Locate and identify every blood parasite.
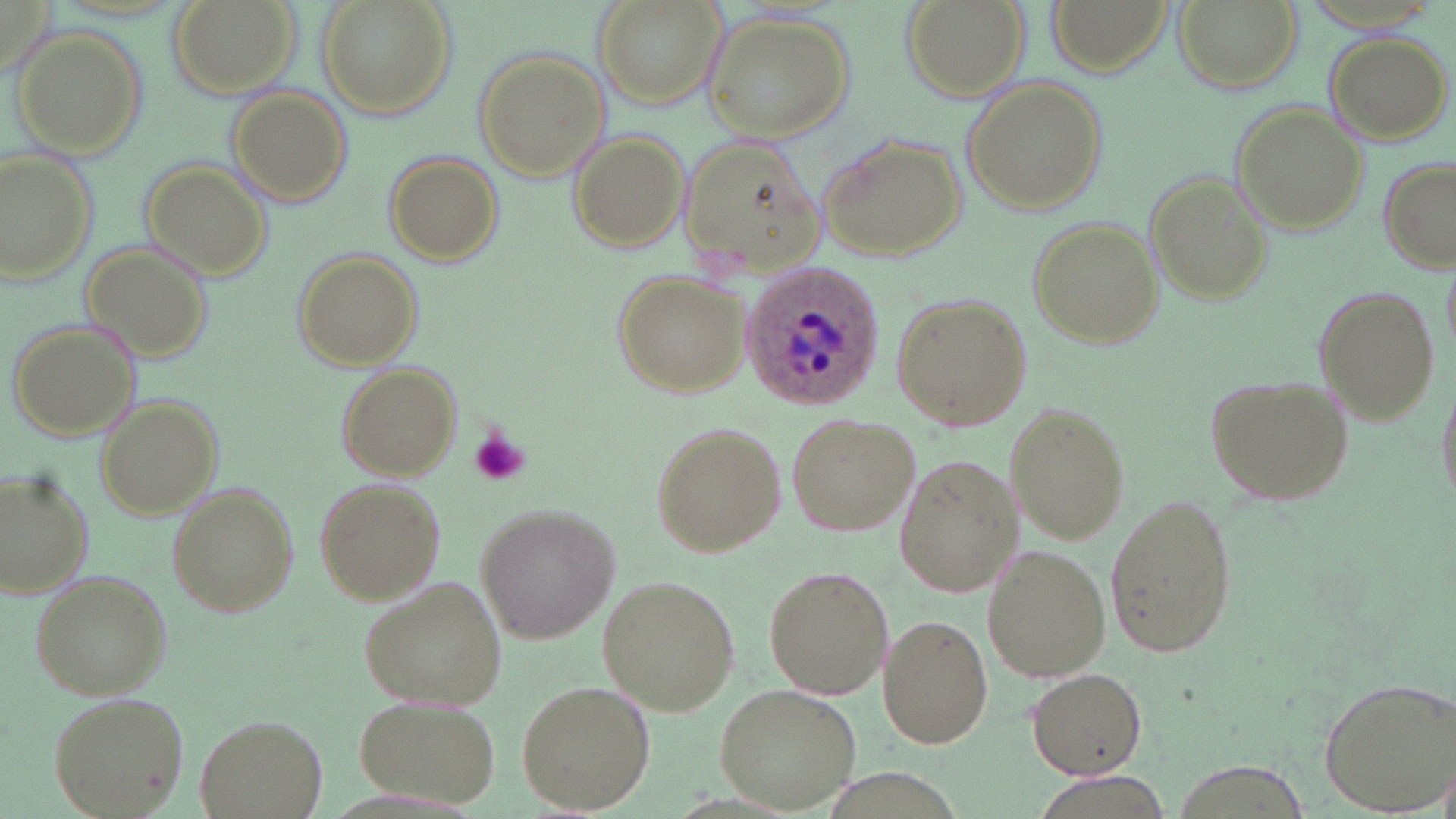
Approximate bounding boxes as (x1,y1)-(x2,y2) corner pairs in pixels.
Plasmodium ovale-infected red blood cells: (738,264)-(886,411).
No Plasmodium falciparum, Plasmodium malariae, Plasmodium vivax, Babesia divergens, or Trypanosoma brucei observed.

Platelet locations: (468,428)-(532,488). Uninfected red blood cell locations: (165,0)-(302,101), (317,0)-(456,118), (593,0)-(729,111), (900,0)-(1031,101), (1047,0)-(1171,77), (1173,0)-(1302,94), (700,6)-(853,142), (15,29)-(148,156), (1325,31)-(1452,145), (471,48)-(611,182), (960,76)-(1108,214), (226,85)-(353,207), (1230,100)-(1366,234), (815,128)-(967,261), (567,131)-(692,253), (676,135)-(826,277), (0,146)-(102,288), (381,150)-(506,267), (1377,155)-(1454,275), (141,157)-(272,280), (1146,172)-(1271,304), (1027,215)-(1163,348), (79,239)-(214,362), (290,247)-(423,371), (612,268)-(751,398), (1310,285)-(1442,425), (891,292)-(1031,434), (7,315)-(141,441), (335,362)-(462,480), (1203,372)-(1354,507), (1435,379)-(1455,509), (93,392)-(223,522), (1003,401)-(1132,546), (784,411)-(919,537), (649,421)-(787,558), (893,453)-(1021,596), (0,468)-(94,599), (308,476)-(446,609), (164,483)-(298,621), (1102,491)-(1240,663), (474,501)-(620,645), (981,544)-(1111,685), (763,564)-(894,699), (28,570)-(169,699), (355,574)-(509,715), (596,574)-(741,716), (877,615)-(993,751), (1026,668)-(1146,780), (1316,675)-(1454,814), (516,677)-(657,813), (713,683)-(861,812), (47,689)-(193,819), (354,696)-(500,806), (196,714)-(327,818). Slide-level diagnosis: Plasmodium ovale. May-Grünwald-Giemsa stain. Single field of view. Thin blood film. 1000x magnification. Image is 1456×819 pixels. Optical microscopy.